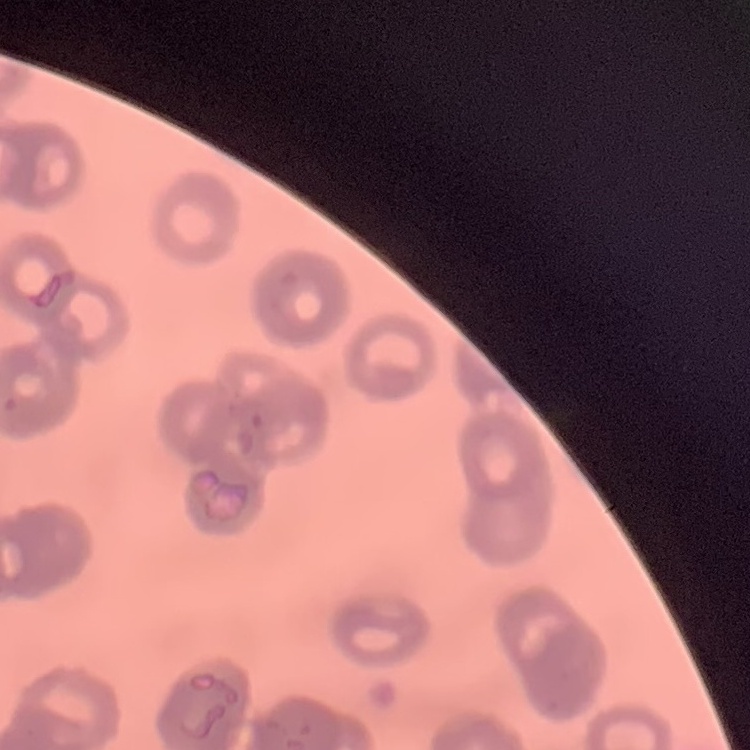
The red blood cells exhibit rouleaux formation. Stained with either Field's or Giemsa. Thin blood smear. Square crop of a larger photomicrograph.